Identify the preparation type.
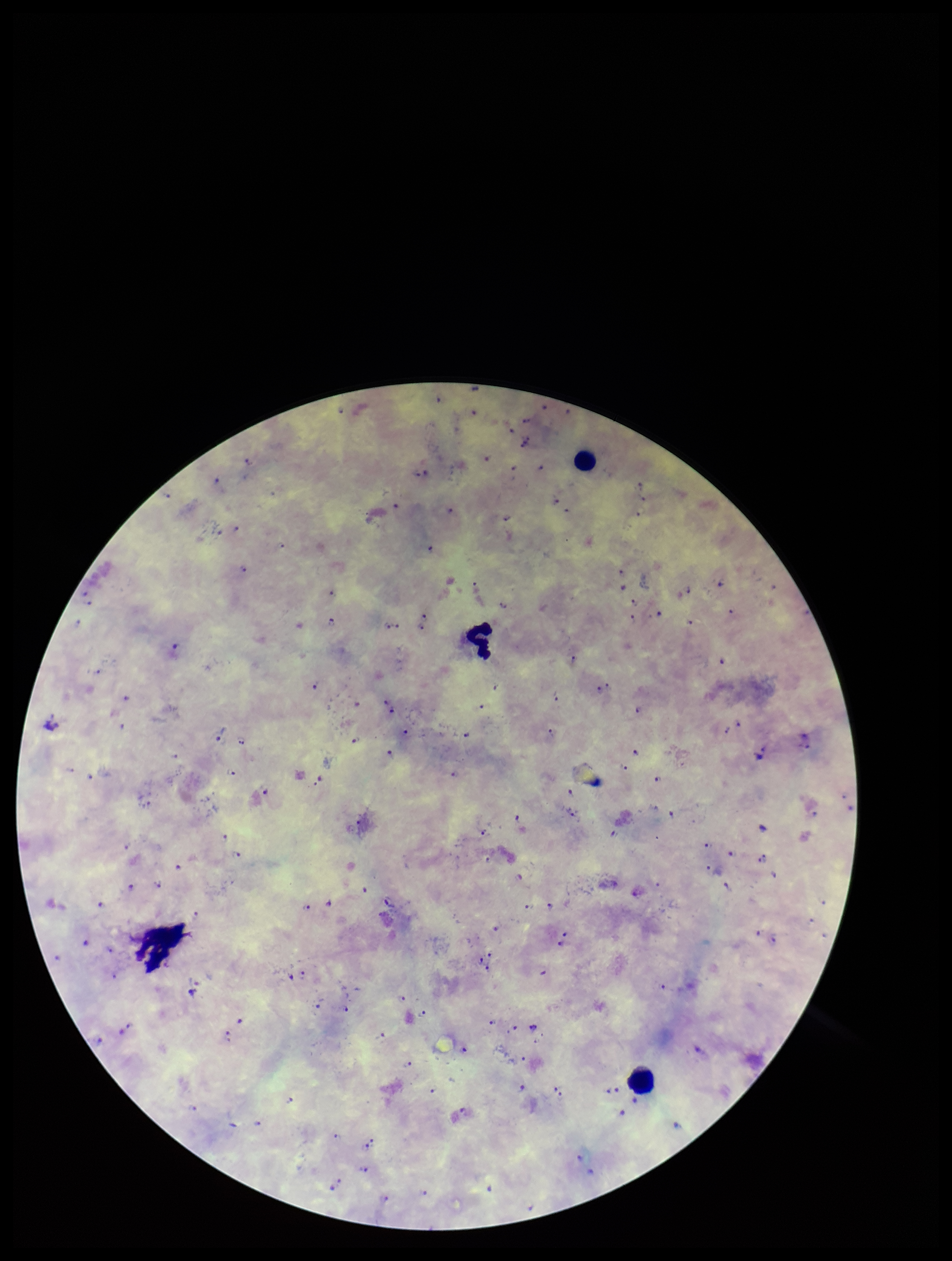
Thick.

Parasite count: 116. Species reported for this patient: Plasmodium falciparum. Single field of view. Image is 952×1261 pixels. Leukocyte count: 4. Giemsa stain. Photographed through the microscope eyepiece with a smartphone camera. Plasmodium parasites: seen. Patient malaria status: infected.